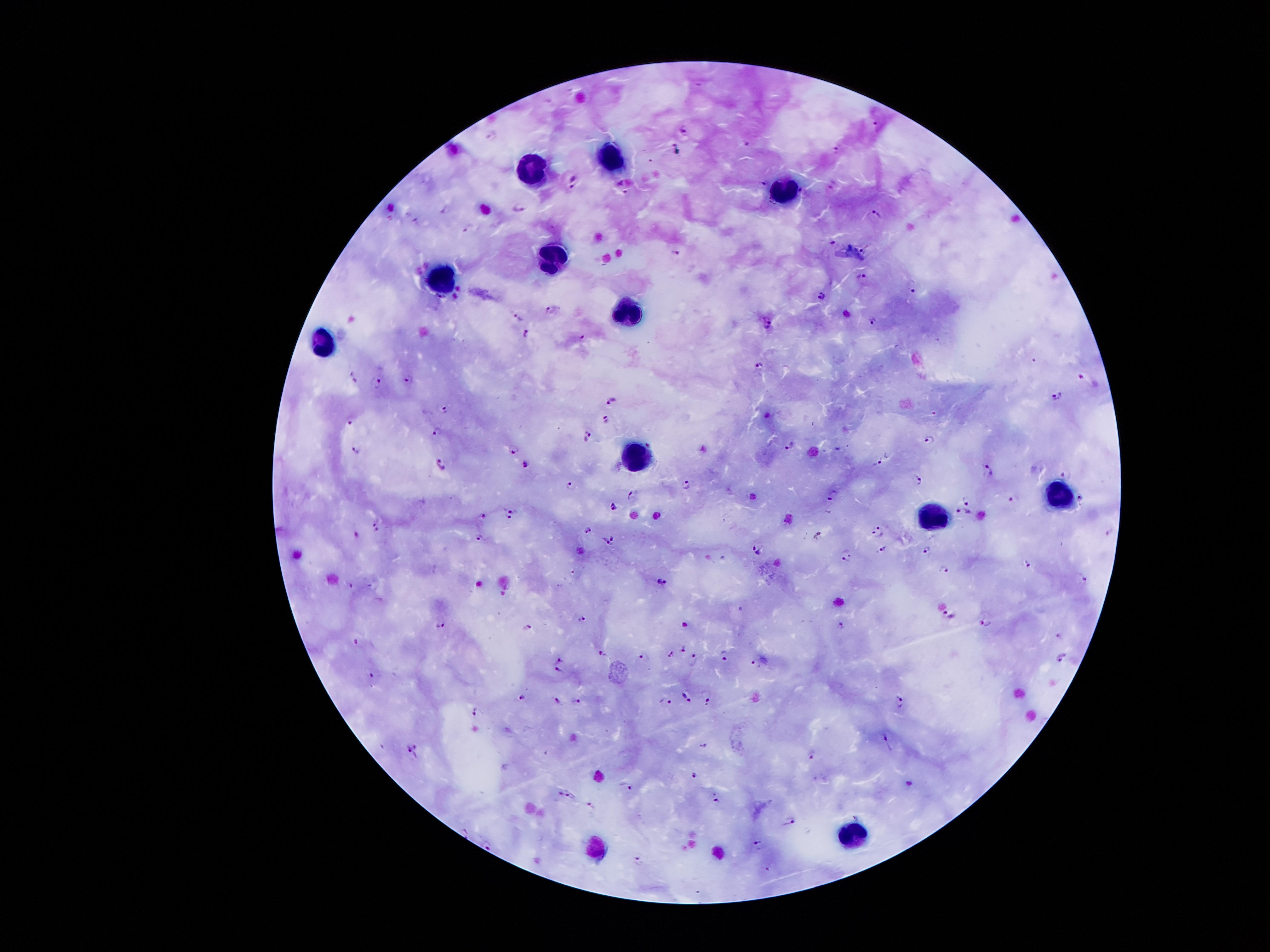
Approximate centers as {x, y} in pixels. Leukocyte locations: {611, 155}, {528, 171}, {782, 192}, {551, 260}, {442, 274}, {634, 315}, {318, 345}, {637, 459}, {1060, 499}, {937, 516}, {846, 838}. Malaria parasite locations: {684, 128}, {491, 134}, {748, 144}, {675, 148}, {835, 150}, {572, 179}, {765, 183}, {834, 184}, {520, 207}, {445, 209}, {875, 213}, {467, 226}, {833, 242}, {864, 249}, {676, 252}, {863, 277}, {913, 287}, {822, 294}, {553, 310}, {518, 316}, {875, 321}, {768, 324}, {528, 333}, {582, 339}, {757, 365}, {354, 374}, {410, 378}, {376, 382}, {1058, 394}, {613, 399}, {444, 408}, {352, 418}, {606, 419}, {438, 431}, {588, 435}, {930, 436}, {649, 444}, {789, 446}, {355, 448}, {515, 449}, {878, 460}, {443, 463}, {527, 464}, {989, 471}, {1067, 476}, {916, 478}, {686, 484}, {570, 486}, {631, 493}, {832, 494}, {1010, 497}, {969, 502}, {613, 505}, {512, 509}, {962, 509}, {484, 513}, {510, 518}, {376, 520}, {587, 528}, {879, 531}, {614, 535}, {479, 538}, {606, 544}, {757, 545}, {884, 549}, {927, 550}, {846, 555}, {1027, 562}, {944, 566}, {1084, 579}, {661, 581}, {351, 585}, {950, 614}, {582, 617}, {985, 620}, {441, 624}, {842, 625}, {528, 626}, {684, 648}, {603, 652}, {671, 654}, {641, 656}, {725, 656}, {1061, 657}, {558, 658}, {693, 659}, {756, 664}, {558, 672}, {371, 674}, {706, 696}, {521, 697}, {687, 697}, {577, 700}, {666, 700}, {557, 701}, {900, 701}, {477, 711}, {889, 741}, {704, 745}, {411, 752}, {813, 753}, {695, 774}, {626, 786}, {568, 794}, {716, 798}, {589, 806}, {854, 819}, {790, 820}, {486, 844}, {761, 844}, {635, 860}. Smartphone photograph taken through the microscope eyepiece. Image is 1270×952 pixels. 100x magnification. Thick peripheral-blood smear. One field from this slide. Giemsa-stained preparation. Patient malaria status: infected with Plasmodium falciparum.